Name the parasite shown.
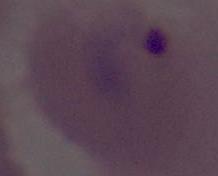

This is Plasmodium.

Summary:
  - Modality: micrograph
  - Magnification: 400x or 1000x